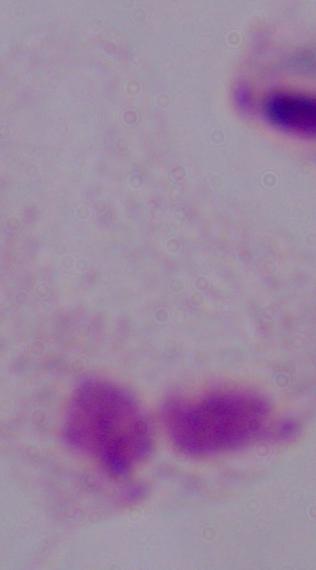

Summary:
  - Identification: trichomonad
  - Magnification: 1000x
  - Modality: photomicrograph